State which cell type is depicted.
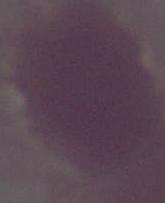

This is an erythrocyte.

{
  "magnification": "1000x",
  "modality": "photomicrograph"
}